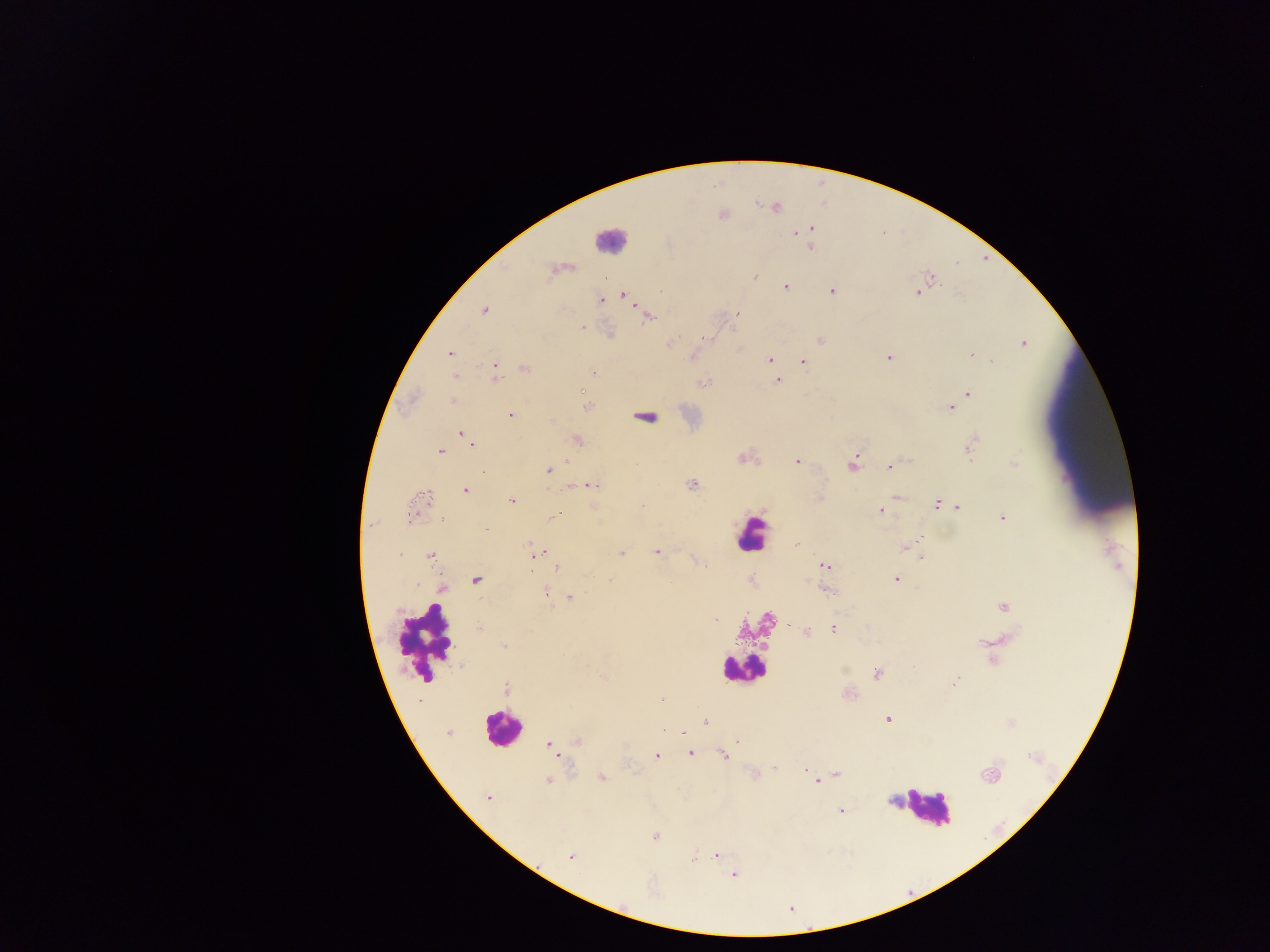
{
  "image_size": "1270×952 pixels",
  "preparation": "thick blood smear",
  "leukocyte_locations": "approximate centers as {x, y} in pixels: {609, 239}, {751, 535}, {423, 642}, {740, 669}, {501, 728}, {926, 806}",
  "plasmodium_parasite_locations": "approximate centers as {x, y} in pixels: {775, 207}, {812, 229}, {796, 233}, {810, 247}, {552, 271}, {754, 277}, {604, 278}, {931, 278}, {785, 287}, {832, 291}, {918, 292}, {624, 296}, {600, 300}, {485, 310}, {737, 315}, {648, 317}, {582, 326}, {707, 339}, {820, 339}, {672, 342}, {1023, 343}, {450, 353}, {971, 354}, {693, 356}, {888, 357}, {770, 358}, {803, 361}, {992, 361}, {773, 366}, {525, 368}, {496, 373}, {593, 373}, {455, 376}, {777, 381}, {704, 383}, {581, 390}, {968, 394}, {453, 401}, {587, 407}, {950, 408}, {510, 415}, {645, 418}, {551, 421}, {461, 433}, {577, 439}, {472, 444}, {970, 446}, {439, 451}, {742, 459}, {797, 461}, {566, 463}, {853, 463}, {1013, 463}, {890, 467}, {549, 470}, {692, 484}, {593, 485}, {572, 486}, {465, 490}, {897, 497}, {512, 500}, {937, 504}, {958, 507}, {881, 510}, {411, 514}, {551, 517}, {1003, 518}, {443, 520}, {371, 524}, {921, 538}, {917, 540}, {796, 545}, {529, 547}, {905, 547}, {657, 552}, {400, 554}, {535, 554}, {621, 554}, {430, 556}, {922, 559}, {825, 566}, {557, 568}, {895, 579}, {475, 580}, {610, 580}, {443, 589}, {545, 590}, {827, 591}, {569, 597}, {1004, 606}, {716, 619}, {479, 629}, {833, 629}, {805, 631}, {504, 646}, {914, 668}, {877, 673}, {603, 677}, {956, 680}, {506, 689}, {662, 699}, {888, 719}, {705, 722}, {683, 732}, {448, 733}, {577, 740}, {737, 741}, {551, 746}, {555, 753}, {690, 753}, {657, 755}, {723, 755}, {775, 768}, {805, 771}, {755, 774}, {838, 774}, {990, 775}, {602, 778}, {548, 781}, {816, 782}, {488, 798}, {891, 800}, {841, 811}, {655, 836}, {716, 854}, {570, 857}, {733, 875}",
  "field_of_view": "single",
  "country": "Ghana",
  "capture": "mobile-phone photograph through a microscope"
}